Give the extent of all Plasmodium ovale-infected red blood cells.
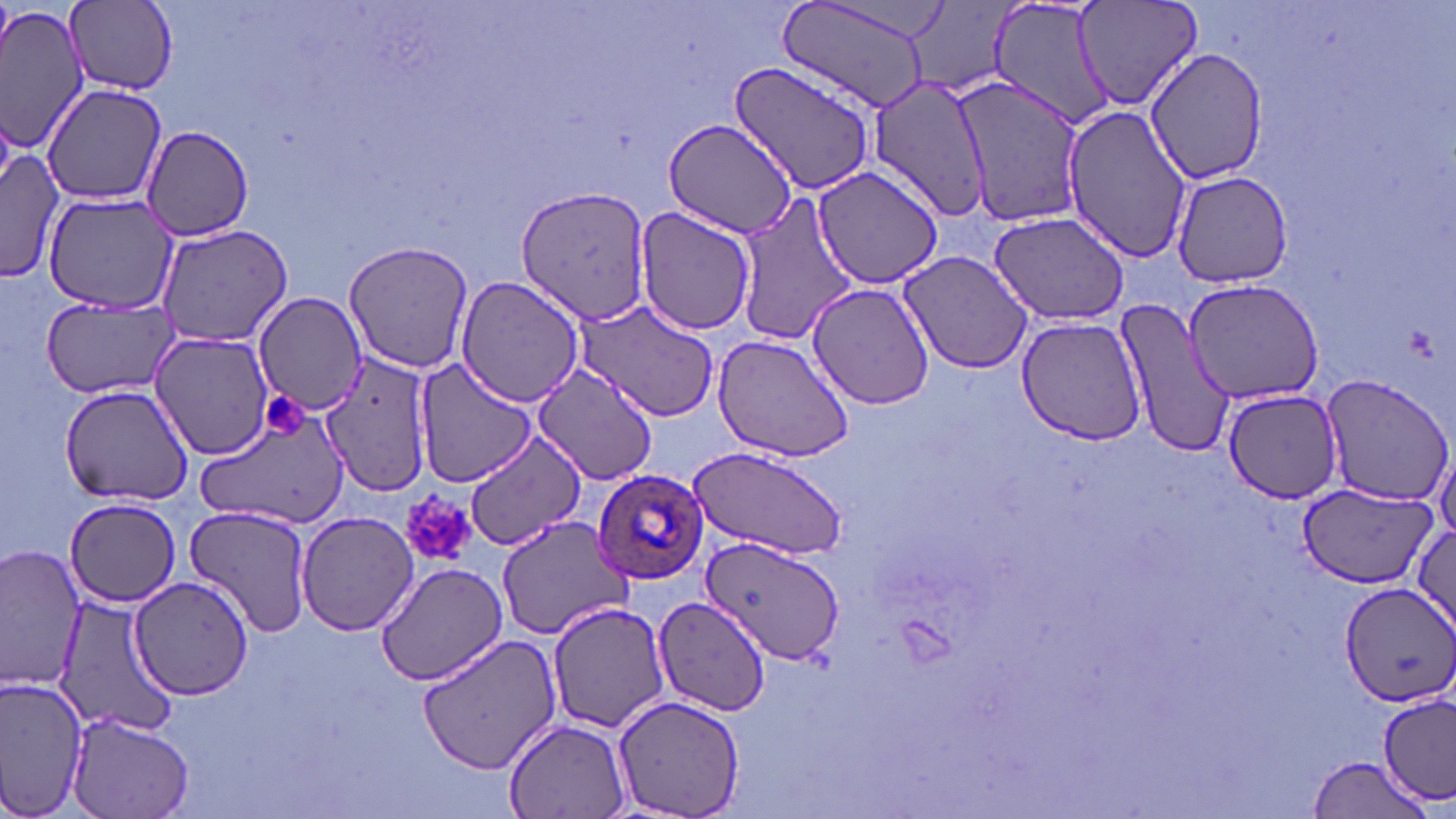

Approximate bounding boxes as named x1/y1/x2/y2 corners in pixels.
Plasmodium ovale-infected red blood cells: (x1=591, y1=467, x2=710, y2=586).

Uninfected red blood cell locations: (x1=1070, y1=0, x2=1208, y2=115), (x1=65, y1=1, x2=179, y2=93), (x1=775, y1=1, x2=938, y2=111), (x1=986, y1=1, x2=1112, y2=131), (x1=0, y1=2, x2=92, y2=156), (x1=1143, y1=45, x2=1271, y2=185), (x1=727, y1=60, x2=879, y2=194), (x1=947, y1=75, x2=1091, y2=226), (x1=866, y1=76, x2=995, y2=219), (x1=40, y1=83, x2=169, y2=204), (x1=1061, y1=106, x2=1194, y2=264), (x1=662, y1=117, x2=802, y2=237), (x1=141, y1=125, x2=254, y2=241), (x1=1, y1=145, x2=65, y2=284), (x1=811, y1=166, x2=947, y2=290), (x1=1170, y1=168, x2=1295, y2=288), (x1=516, y1=184, x2=656, y2=328), (x1=41, y1=193, x2=176, y2=316), (x1=733, y1=194, x2=857, y2=349), (x1=634, y1=207, x2=757, y2=337), (x1=987, y1=209, x2=1132, y2=326), (x1=154, y1=223, x2=295, y2=348), (x1=342, y1=239, x2=475, y2=375), (x1=897, y1=250, x2=1034, y2=375), (x1=455, y1=276, x2=585, y2=408), (x1=1184, y1=279, x2=1324, y2=404), (x1=806, y1=282, x2=934, y2=412), (x1=252, y1=291, x2=368, y2=414), (x1=40, y1=294, x2=183, y2=400), (x1=1112, y1=296, x2=1237, y2=459), (x1=574, y1=299, x2=718, y2=422), (x1=1015, y1=316, x2=1146, y2=445), (x1=150, y1=331, x2=276, y2=460), (x1=712, y1=334, x2=854, y2=463), (x1=322, y1=352, x2=434, y2=495), (x1=414, y1=358, x2=536, y2=487), (x1=529, y1=361, x2=661, y2=484), (x1=1321, y1=375, x2=1456, y2=506), (x1=59, y1=383, x2=195, y2=505), (x1=1223, y1=389, x2=1346, y2=503), (x1=194, y1=410, x2=347, y2=527), (x1=466, y1=429, x2=587, y2=553), (x1=1432, y1=440, x2=1455, y2=542), (x1=686, y1=445, x2=850, y2=561), (x1=1296, y1=481, x2=1435, y2=583), (x1=63, y1=498, x2=181, y2=606), (x1=185, y1=504, x2=315, y2=638), (x1=296, y1=511, x2=423, y2=636), (x1=497, y1=517, x2=635, y2=641), (x1=1410, y1=520, x2=1456, y2=633), (x1=701, y1=534, x2=843, y2=666), (x1=1, y1=545, x2=88, y2=694), (x1=375, y1=561, x2=509, y2=685), (x1=130, y1=575, x2=256, y2=699), (x1=1338, y1=581, x2=1456, y2=708), (x1=50, y1=594, x2=183, y2=737), (x1=652, y1=600, x2=768, y2=718), (x1=547, y1=602, x2=669, y2=734), (x1=417, y1=631, x2=564, y2=775), (x1=0, y1=674, x2=88, y2=819), (x1=613, y1=694, x2=745, y2=818), (x1=1378, y1=695, x2=1455, y2=804), (x1=68, y1=711, x2=195, y2=819), (x1=503, y1=717, x2=631, y2=819), (x1=1304, y1=756, x2=1436, y2=818). Platelet locations: (x1=263, y1=394, x2=306, y2=436), (x1=400, y1=492, x2=475, y2=569). Slide-level diagnosis: Plasmodium ovale. May-Grünwald-Giemsa-stained preparation. 1000x magnification. Light microscopy. Thin blood film. Image is 1456×819 pixels. One field of a larger specimen.